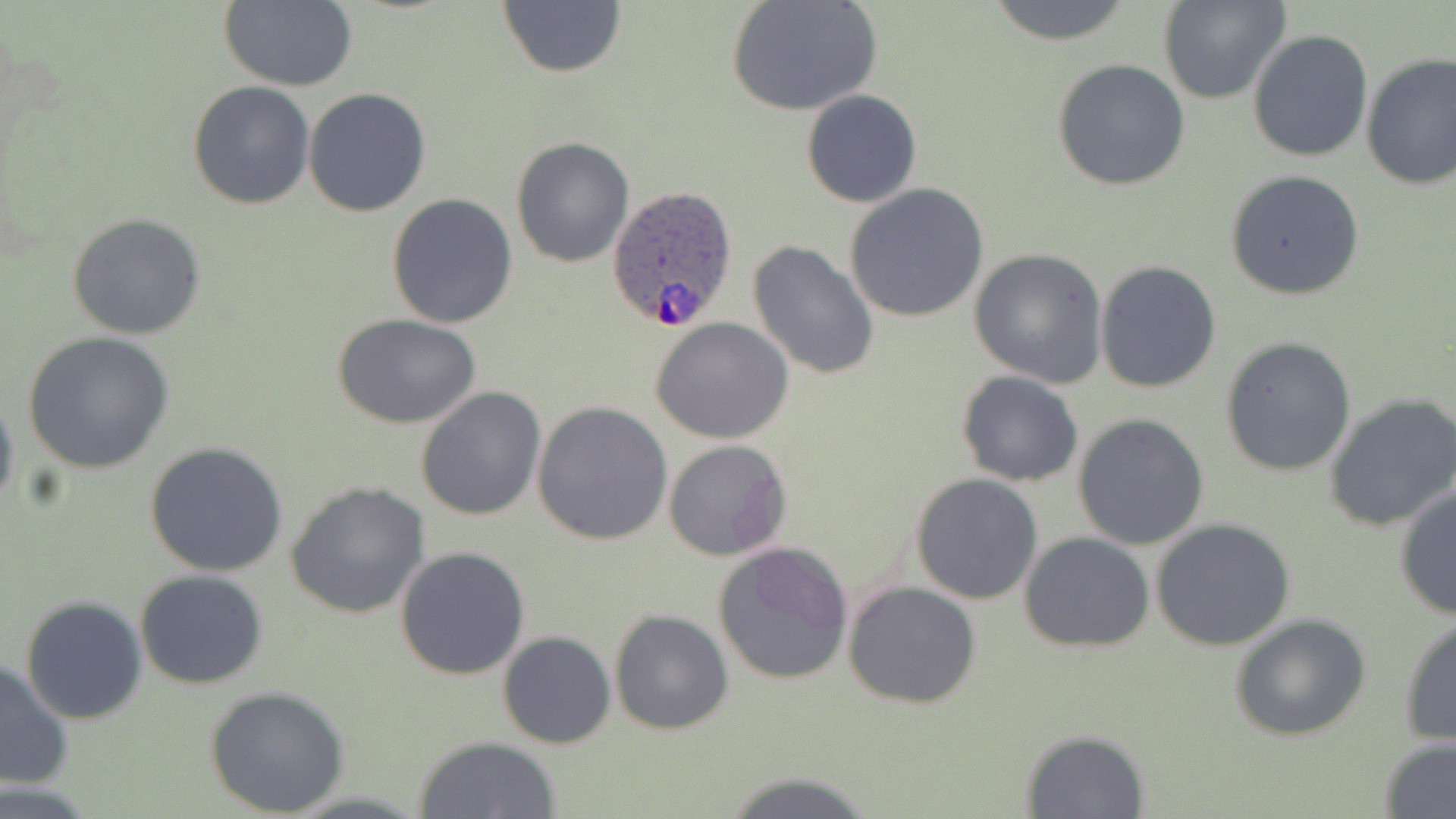

Summary:
  - Coordinate format: approximate bounding boxes as (x1,y1)-(x2,y2) corner pairs in pixels
  - Plasmodium ovale-infected red blood cell locations: (608,185)-(739,331)
  - Uninfected red blood cell locations: (725,0)-(881,117), (218,1)-(357,92), (981,1)-(1139,46), (1157,1)-(1291,105), (497,2)-(627,79), (1247,28)-(1373,163), (1360,53)-(1456,193), (1051,59)-(1190,190), (187,81)-(315,210), (303,87)-(432,216), (801,91)-(922,208), (510,138)-(634,267), (1224,168)-(1366,301), (843,183)-(989,324), (387,192)-(518,327), (67,212)-(205,339), (748,240)-(880,379), (969,248)-(1108,388), (1094,261)-(1222,393), (335,313)-(482,429), (651,317)-(794,444), (23,331)-(175,474), (1220,337)-(1356,476), (956,371)-(1083,487), (0,386)-(19,522), (415,386)-(546,521), (1325,392)-(1456,531), (534,401)-(674,544), (1072,414)-(1210,550), (663,439)-(791,562), (146,443)-(289,578), (910,475)-(1044,605), (286,482)-(430,619), (1393,483)-(1456,621), (1152,518)-(1298,651), (1018,531)-(1155,653), (713,542)-(854,686), (394,548)-(531,680), (134,569)-(269,689), (843,580)-(983,708), (21,596)-(149,724), (609,609)-(733,735), (1230,612)-(1371,741), (1397,615)-(1455,747), (498,631)-(615,748), (0,659)-(75,790), (205,685)-(351,816), (1021,729)-(1151,817), (413,735)-(563,818), (1378,740)-(1456,818), (716,769)-(882,819)
  - Slide-level diagnosis: Plasmodium ovale
  - Field of view: one of a larger specimen
  - Image size: 1456×819 pixels
  - Preparation: thin blood film
  - Stain: May-Grünwald-Giemsa
  - Magnification: 1000x
  - Modality: optical microscopy